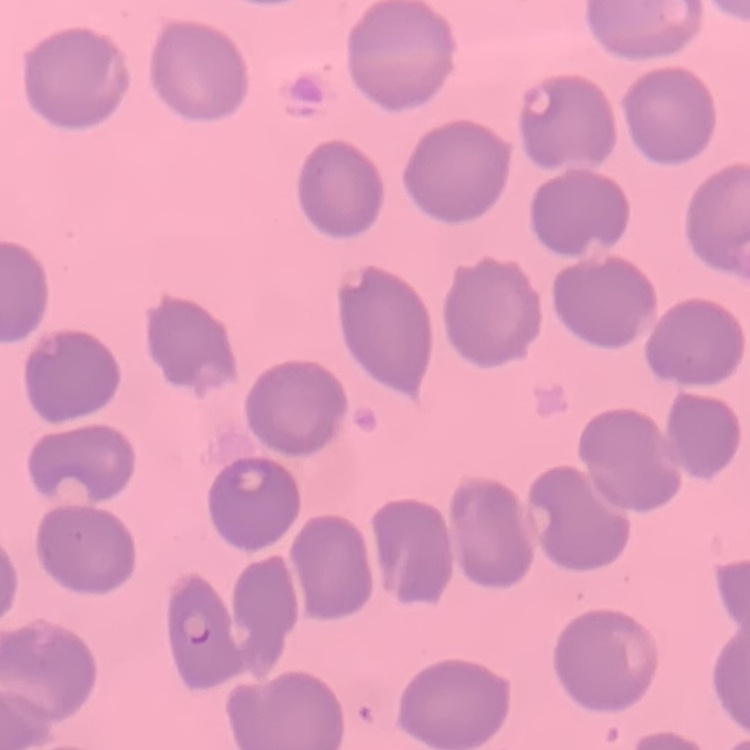
The red blood cells show no rouleaux formation. Stained with either Field's or Giemsa. One tile cut from a larger photomicrograph. Thin peripheral smear.